Assess this cell for malaria.
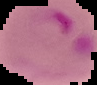

It is parasitized.

Image is 97×85 pixels. From a thin blood film. Segmented cell region on a black background.